Locate the cells, classifying each as a parasitized red blood cell, an uninfected red blood cell, or a white blood cell.
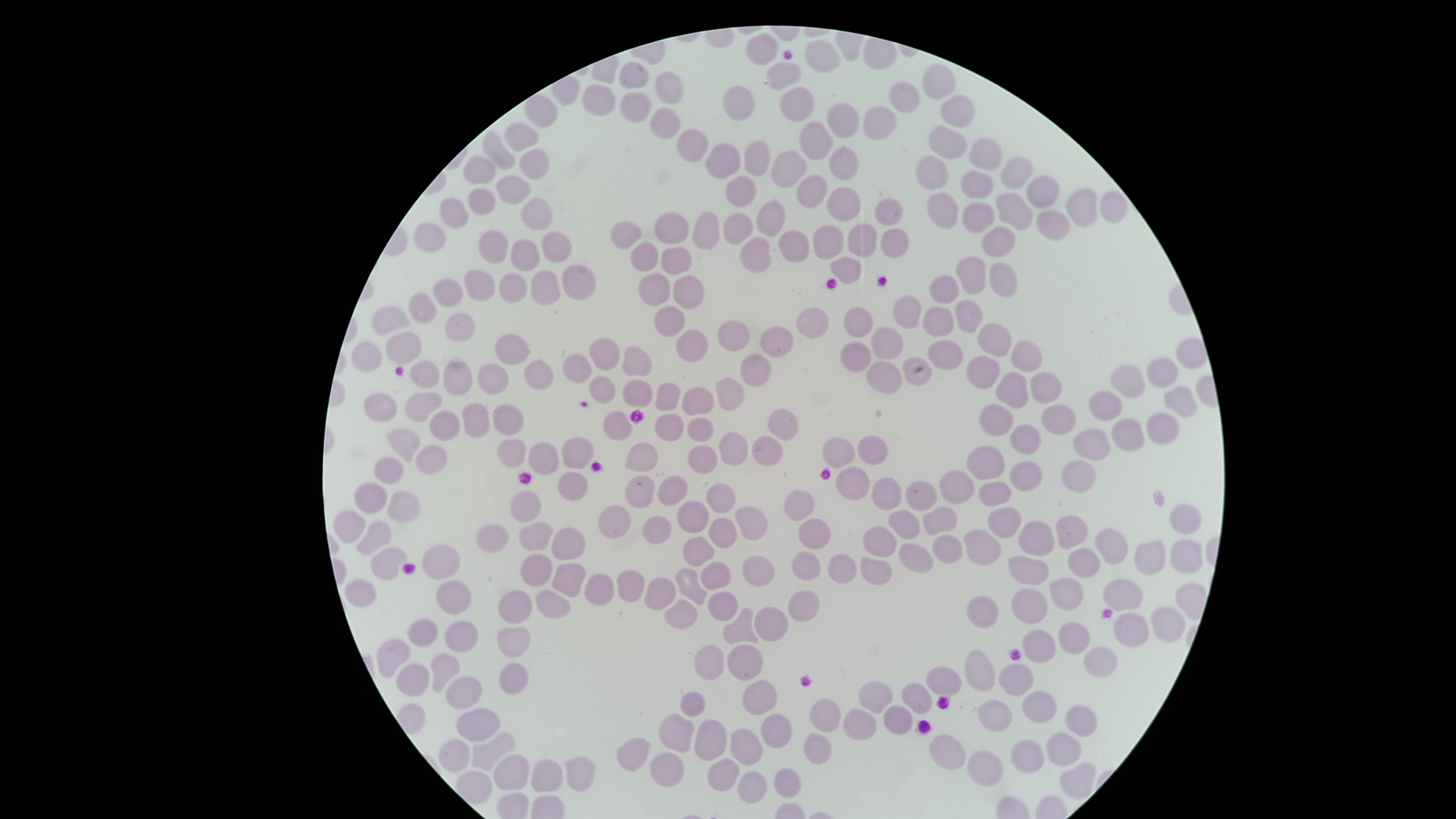

No parasitized red blood cells identified.
Approximate marker points, in pixels from the top-left corner.
Uninfected red blood cells: (x=762, y=44), (x=823, y=57), (x=783, y=73), (x=636, y=74), (x=671, y=84), (x=937, y=85), (x=599, y=96), (x=794, y=99), (x=736, y=100), (x=903, y=101), (x=636, y=104), (x=541, y=111), (x=955, y=113), (x=842, y=119), (x=663, y=123), (x=872, y=127), (x=517, y=133), (x=816, y=137), (x=948, y=143), (x=688, y=147), (x=494, y=151), (x=983, y=154), (x=530, y=156), (x=722, y=156), (x=753, y=156), (x=843, y=160), (x=791, y=165), (x=482, y=167), (x=1018, y=171), (x=935, y=172), (x=975, y=185), (x=738, y=188), (x=513, y=189), (x=1041, y=189), (x=815, y=190), (x=474, y=198), (x=1012, y=202), (x=839, y=204), (x=1080, y=207), (x=1115, y=207), (x=454, y=210), (x=539, y=210), (x=881, y=210), (x=944, y=212), (x=975, y=215), (x=771, y=220), (x=1048, y=224), (x=669, y=227), (x=738, y=227), (x=706, y=230), (x=629, y=233), (x=824, y=236), (x=424, y=237), (x=887, y=237), (x=853, y=239), (x=997, y=239), (x=490, y=240), (x=556, y=242), (x=797, y=243), (x=521, y=254), (x=755, y=257), (x=642, y=259), (x=674, y=261), (x=845, y=265), (x=972, y=272), (x=1000, y=274), (x=579, y=277), (x=478, y=281), (x=540, y=281), (x=693, y=285), (x=515, y=286), (x=943, y=289), (x=654, y=292), (x=448, y=295), (x=422, y=305), (x=907, y=311), (x=975, y=313), (x=393, y=317), (x=852, y=317), (x=933, y=317), (x=665, y=318), (x=813, y=319), (x=461, y=325), (x=727, y=333), (x=778, y=337), (x=887, y=337), (x=987, y=337), (x=398, y=343), (x=684, y=349), (x=369, y=350), (x=513, y=350), (x=604, y=353), (x=1022, y=355), (x=856, y=356), (x=940, y=356), (x=635, y=361), (x=573, y=365), (x=1159, y=367), (x=761, y=370), (x=980, y=370), (x=425, y=374), (x=536, y=374), (x=1130, y=374), (x=883, y=375), (x=456, y=377), (x=917, y=378), (x=492, y=380), (x=1041, y=385), (x=604, y=386), (x=1012, y=387), (x=726, y=390), (x=637, y=392), (x=1181, y=394), (x=695, y=396), (x=382, y=401), (x=663, y=401), (x=418, y=403), (x=1101, y=409), (x=514, y=414), (x=615, y=418), (x=995, y=418), (x=1058, y=418), (x=472, y=419), (x=669, y=422), (x=784, y=423), (x=1157, y=425), (x=441, y=426), (x=701, y=426), (x=1120, y=432), (x=1022, y=440), (x=409, y=443), (x=871, y=443), (x=1087, y=443), (x=764, y=445), (x=728, y=449), (x=510, y=450), (x=573, y=454), (x=835, y=454), (x=543, y=455), (x=637, y=456), (x=701, y=457), (x=426, y=458), (x=984, y=461), (x=1022, y=468), (x=388, y=469), (x=1073, y=471), (x=951, y=481), (x=854, y=483), (x=572, y=485), (x=665, y=486), (x=889, y=488), (x=635, y=492), (x=993, y=492), (x=915, y=493), (x=370, y=495), (x=718, y=500), (x=400, y=504), (x=530, y=507), (x=801, y=507), (x=689, y=512), (x=1182, y=515), (x=616, y=518), (x=942, y=519), (x=1001, y=520), (x=904, y=521), (x=352, y=523), (x=746, y=523), (x=657, y=525), (x=1070, y=532), (x=499, y=534), (x=536, y=534), (x=719, y=535), (x=1037, y=537), (x=880, y=538), (x=372, y=541), (x=812, y=541), (x=572, y=542), (x=980, y=543), (x=1113, y=546), (x=932, y=550), (x=697, y=552), (x=1187, y=556), (x=1150, y=558), (x=907, y=559), (x=1077, y=563), (x=380, y=564), (x=434, y=566), (x=536, y=568), (x=842, y=568), (x=871, y=568), (x=802, y=570), (x=1029, y=570), (x=756, y=571), (x=713, y=573), (x=561, y=574), (x=685, y=584), (x=625, y=585), (x=593, y=589), (x=358, y=592), (x=1062, y=592), (x=1122, y=592), (x=659, y=594), (x=454, y=597), (x=806, y=602), (x=511, y=603), (x=554, y=603), (x=723, y=604), (x=1029, y=604), (x=678, y=608), (x=980, y=613), (x=1160, y=623), (x=774, y=624), (x=1125, y=628), (x=736, y=630), (x=423, y=631), (x=516, y=631), (x=463, y=635), (x=1037, y=639), (x=1074, y=639), (x=396, y=651), (x=704, y=659), (x=1103, y=659), (x=977, y=665), (x=747, y=667), (x=447, y=668), (x=511, y=671), (x=1020, y=677), (x=950, y=678), (x=411, y=682), (x=467, y=693), (x=872, y=696), (x=762, y=697), (x=916, y=697), (x=692, y=705), (x=1037, y=710), (x=992, y=715), (x=818, y=716), (x=855, y=722), (x=897, y=722), (x=1073, y=722), (x=480, y=724), (x=781, y=731), (x=676, y=736), (x=705, y=738), (x=752, y=741), (x=451, y=746), (x=1056, y=748), (x=491, y=751), (x=814, y=752), (x=945, y=752), (x=626, y=758), (x=1025, y=759), (x=666, y=767), (x=509, y=772), (x=548, y=772), (x=580, y=772), (x=986, y=773), (x=725, y=776), (x=1074, y=777), (x=782, y=780), (x=749, y=787).
No white blood cells identified.

Thin blood film. Single field of view. Giemsa stain. Image is 1456×819 pixels. Circular visible region. Smartphone photograph through the microscope eyepiece.